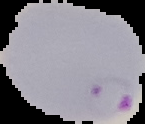
Summary:
  - Preparation: thin blood smear
  - Result: malaria parasites detected
  - Image type: segmented cell region with the area outside set to black
  - Image size: 145×124 pixels